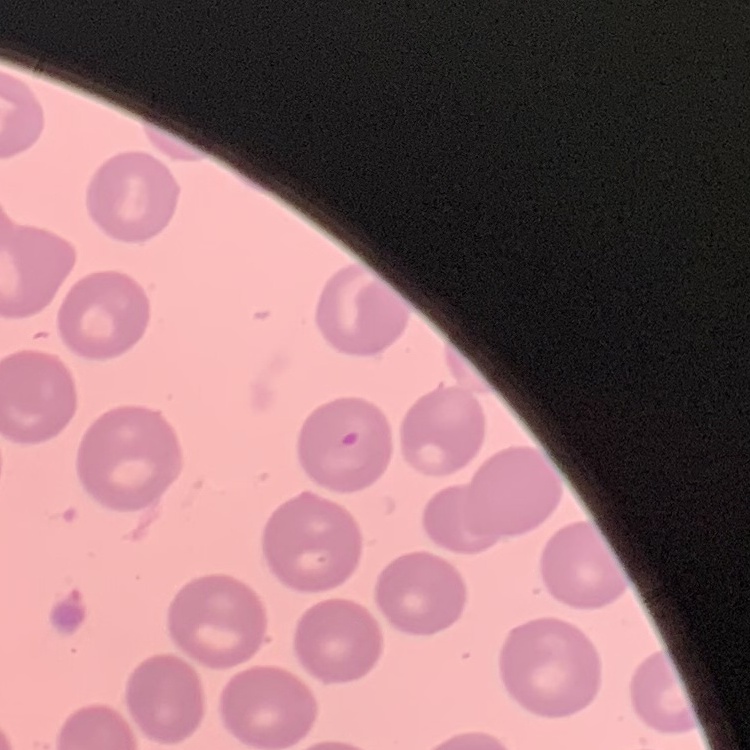

The erythrocytes show no rouleaux formation. One tile cut from a larger photomicrograph. Stained with either Field's or Giemsa. Thin blood film.